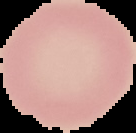
image type = cell region segmented out of the field of view; surrounding area masked to black
image size = 136×133 pixels
preparation = thin blood smear
malaria status = uninfected